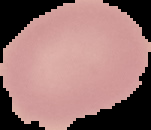
image size = 151×130 pixels
image type = segmented cell region with the area outside set to black
preparation = thin blood smear
result = negative for malaria parasites